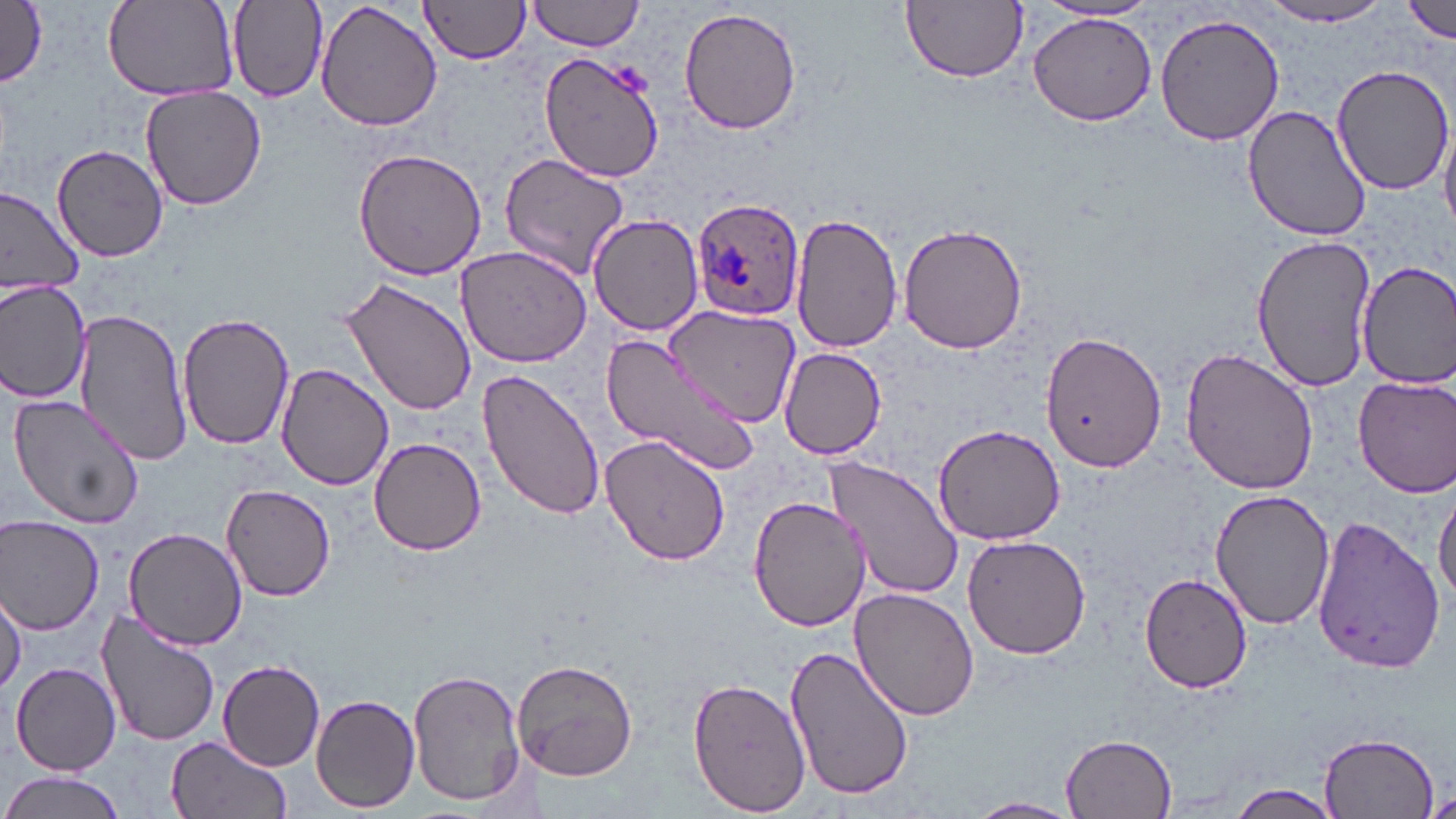
Summary:
  - Coordinate format: approximate bounding boxes as [x1, y1, x2, y2] in pixels
  - Uninfected red blood cell locations: [0, 0, 49, 90], [103, 0, 239, 99], [230, 0, 327, 100], [314, 0, 443, 133], [526, 0, 650, 52], [904, 0, 1028, 83], [420, 1, 534, 64], [1402, 1, 1456, 42], [1037, 2, 1159, 25], [1256, 3, 1398, 28], [677, 5, 803, 137], [1028, 11, 1159, 127], [1155, 12, 1284, 147], [540, 51, 666, 183], [1331, 64, 1454, 194], [141, 85, 268, 210], [1244, 104, 1372, 242], [1439, 113, 1456, 237], [51, 143, 168, 262], [353, 147, 488, 283], [500, 154, 631, 279], [0, 188, 82, 295], [790, 212, 904, 356], [590, 214, 705, 337], [898, 221, 1029, 356], [1251, 235, 1377, 391], [455, 243, 593, 367], [1355, 259, 1456, 388], [339, 276, 478, 418], [0, 280, 92, 405], [666, 302, 804, 427], [74, 308, 189, 465], [179, 311, 297, 450], [1041, 330, 1166, 473], [599, 333, 759, 477], [1179, 345, 1319, 494], [778, 347, 886, 460], [275, 361, 396, 490], [480, 368, 606, 522], [1353, 375, 1456, 496], [8, 391, 146, 532], [935, 422, 1065, 544], [599, 432, 732, 567], [368, 435, 489, 556], [825, 458, 964, 602], [219, 483, 339, 602], [1434, 483, 1456, 610], [1209, 488, 1334, 631], [746, 492, 872, 634], [1311, 516, 1445, 675], [1, 517, 104, 633], [122, 526, 249, 650], [962, 534, 1093, 660], [1141, 572, 1253, 693], [1, 585, 26, 696], [848, 586, 982, 722], [94, 606, 222, 749], [783, 644, 916, 802], [513, 657, 638, 782], [216, 658, 325, 770], [10, 663, 120, 775], [408, 667, 525, 808], [688, 675, 812, 816], [311, 692, 421, 813], [1321, 731, 1441, 818], [1062, 732, 1179, 818], [165, 736, 290, 819], [0, 771, 127, 819], [1226, 781, 1347, 819], [967, 796, 1081, 818]
  - Plasmodium ovale-infected red blood cell locations: [689, 195, 806, 322]
  - Platelet locations: [1426, 789, 1456, 819]
  - Slide-level diagnosis: Plasmodium ovale
  - Stain: May-Grünwald-Giemsa
  - Preparation: thin blood smear
  - Modality: optical microscopy
  - Image size: 1456×819 pixels
  - Field of view: single
  - Magnification: 1000x